Classify this cell by malaria status.
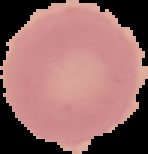

Uninfected.

From a thin blood smear. Segmented cell region on a black background. Image is 148×154 pixels.